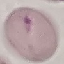

Summary:
  - Result: negative for malaria parasites
  - Preparation: thin smear
  - Stain: Giemsa
  - Capture: smartphone through the microscope eyepiece
  - Image type: cell patch, automatically extracted from a larger field of view and resized to 64 × 64 pixels